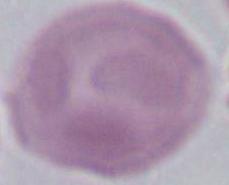
Summary:
  - Magnification: 1000x
  - Modality: micrograph
  - Identification: red blood cell